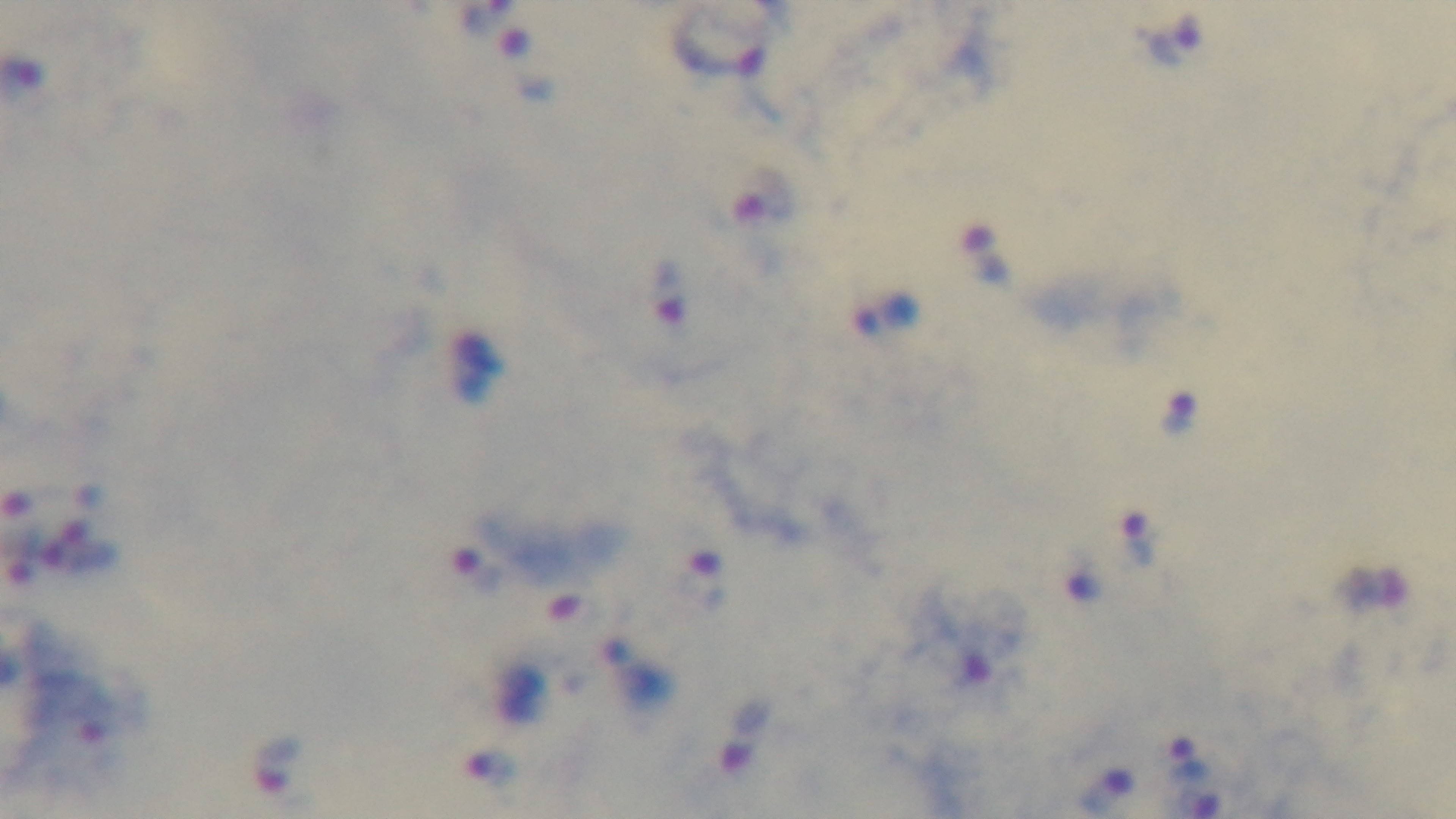

Summary:
  - Field of view: single
  - Objective: 100x oil immersion
  - Stain: Giemsa
  - Modality: light microscopy
  - Capture: mounted 4K digital camera
  - Preparation: thick smear
  - Malaria status: infected